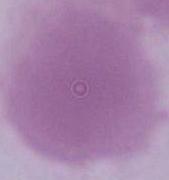
Summary:
  - Modality: photomicrograph
  - Magnification: 1000x
  - Identification: red blood cell